Locate every Plasmodium falciparum-infected red blood cell.
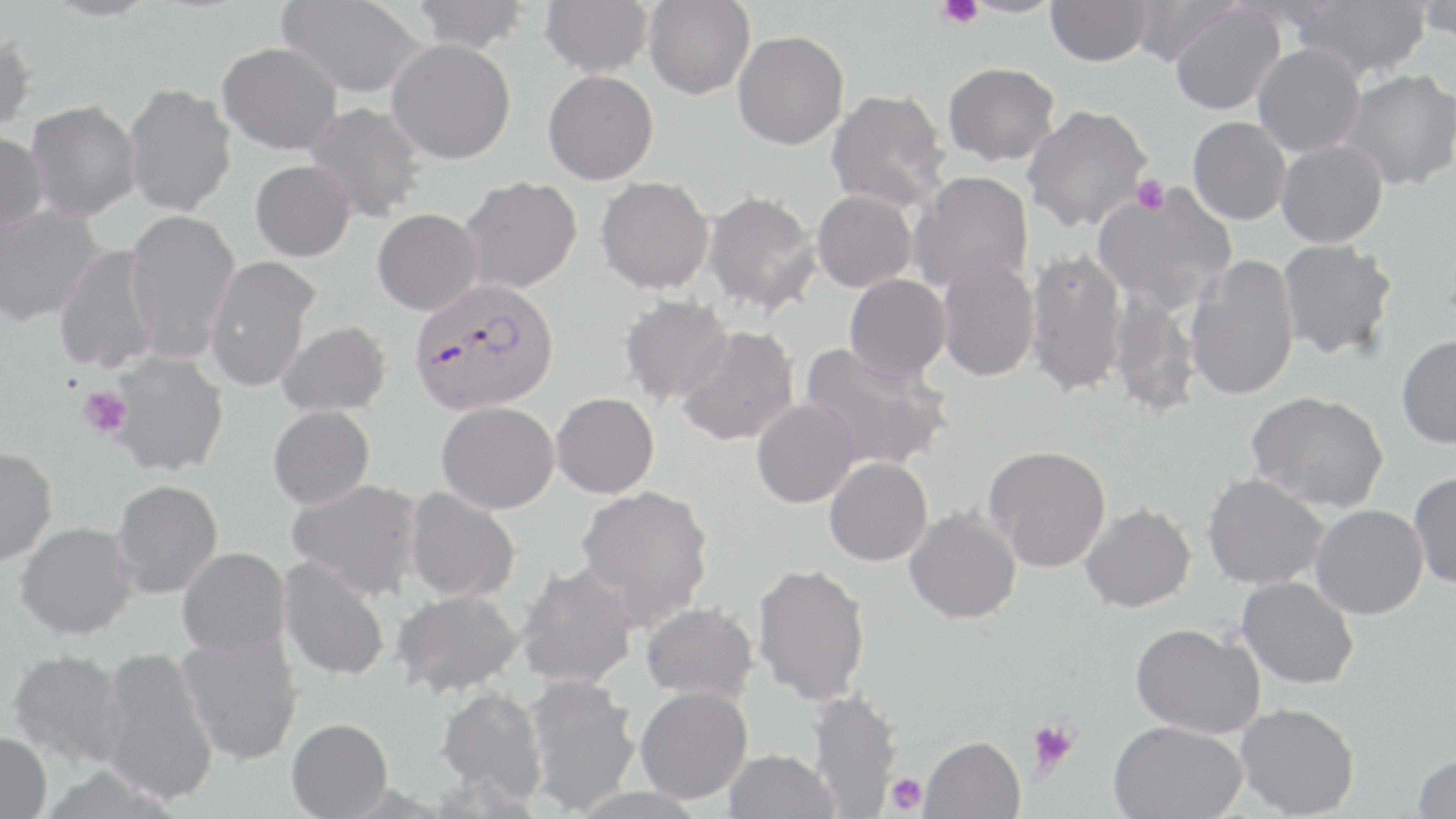

Approximate bounding boxes as (x1,y1)-(x2,y2) corner pairs in pixels.
Plasmodium falciparum-infected red blood cells: (409,277)-(560,417).

slide_level_diagnosis: Plasmodium falciparum
platelet_locations: 'approximate bounding boxes as (x1,y1)-(x2,y2) corner pairs in pixels: (935,0)-(982,28), (1132,175)-(1170,214), (78,387)-(132,438), (1028,719)-(1079,775), (885,773)-(928,815)'
field_of_view: one of a larger specimen
magnification: 1000x
image_size: 1456×819 pixels
preparation: thin blood smear
uninfected_red_blood_cell_locations: 'approximate bounding boxes as (x1,y1)-(x2,y2) corner pairs in pixels: (41,0)-(159,22), (277,0)-(427,99), (411,0)-(529,53), (540,0)-(653,77), (959,0)-(1065,18), (1046,0)-(1154,66), (1129,0)-(1239,68), (1292,0)-(1431,81), (1415,0)-(1455,44), (644,1)-(754,99), (1169,4)-(1285,116), (732,30)-(848,149), (0,32)-(38,136), (386,38)-(516,164), (216,41)-(343,155), (1252,44)-(1365,157), (943,62)-(1060,165), (1337,69)-(1456,191), (542,70)-(658,185), (123,81)-(237,217), (826,90)-(948,213), (26,99)-(141,222), (304,102)-(427,222), (1021,104)-(1152,232), (1187,116)-(1291,225), (0,130)-(49,237), (1275,140)-(1388,248), (250,160)-(356,262), (908,170)-(1033,293), (458,175)-(582,294), (595,176)-(714,294), (1092,184)-(1238,315), (701,190)-(822,316), (811,190)-(918,292), (0,204)-(106,327), (125,208)-(240,362), (372,208)-(483,316), (1277,239)-(1398,360), (53,244)-(161,373), (1025,247)-(1128,398), (203,256)-(321,391), (1185,256)-(1300,401), (936,261)-(1040,381), (844,274)-(951,382), (1108,291)-(1201,417), (619,295)-(733,406), (276,320)-(391,417), (676,326)-(799,446), (1396,335)-(1456,449), (798,342)-(953,471), (107,351)-(229,476), (1246,390)-(1389,513), (551,393)-(659,499), (751,398)-(860,508), (436,401)-(560,514), (268,405)-(375,510), (984,444)-(1111,572), (0,446)-(57,566), (824,456)-(933,565), (1409,471)-(1456,589), (1202,472)-(1328,590), (112,479)-(224,598), (287,479)-(424,600), (574,484)-(714,629), (404,487)-(521,603), (1079,502)-(1196,613), (1310,504)-(1427,619), (904,508)-(1021,624), (15,521)-(137,639), (177,547)-(291,659), (278,555)-(391,682), (515,562)-(639,689), (751,563)-(871,705), (1236,576)-(1359,689), (391,588)-(524,698), (640,602)-(759,703), (1129,622)-(1265,738), (176,634)-(303,766), (99,646)-(219,806), (6,648)-(126,769), (523,673)-(642,814), (436,685)-(548,803), (634,685)-(752,804), (808,689)-(902,818), (1235,702)-(1360,818), (286,717)-(392,818), (1108,719)-(1247,819), (0,731)-(52,819), (920,735)-(1026,819), (723,750)-(840,819), (1411,751)-(1456,819)'
modality: optical microscopy
stain: May-Grünwald-Giemsa